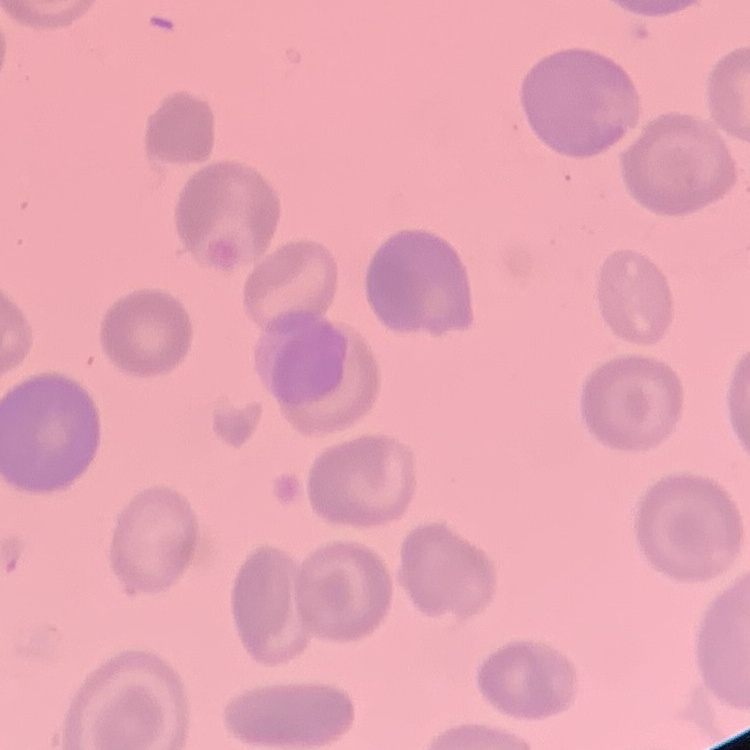

Summary:
  - Erythrocyte morphology: no rouleaux formation
  - Stain: Field's or Giemsa
  - Preparation: thin peripheral smear
  - Image type: one tile cut from a larger photomicrograph